Comment on the morphology of the erythrocytes.
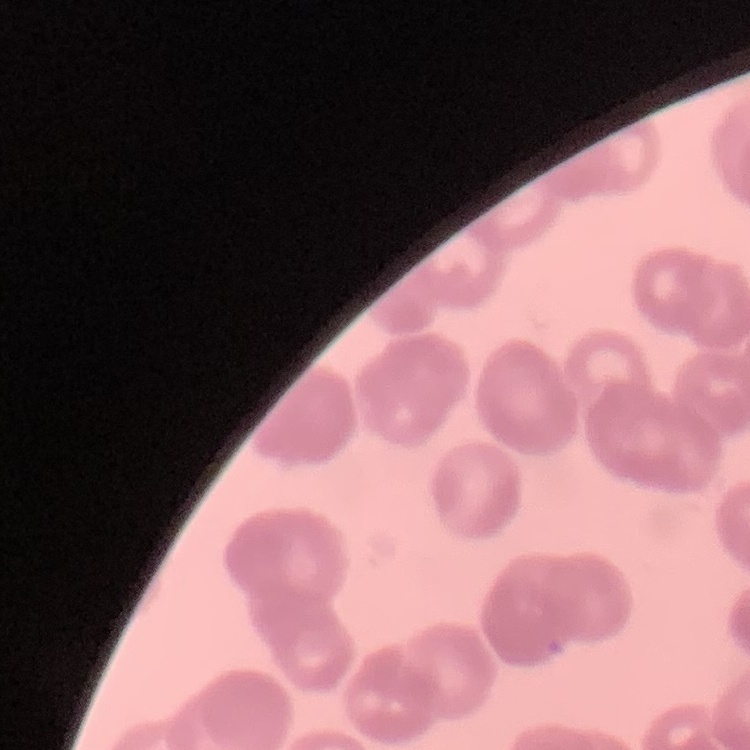
Rouleaux formation.

Stained with either Field's or Giemsa. Thin blood film. Square crop of a larger photomicrograph.